Identify the cell.
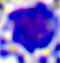

This is a leukocyte.

{
  "magnification": "400x",
  "modality": "micrograph"
}